Assess this cell for malaria.
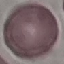
Uninfected.

Summary:
  - Stain: Giemsa
  - Image type: automatically extracted cell patch, resized to 64 × 64 pixels
  - Capture: smartphone through the microscope eyepiece
  - Preparation: thin blood film